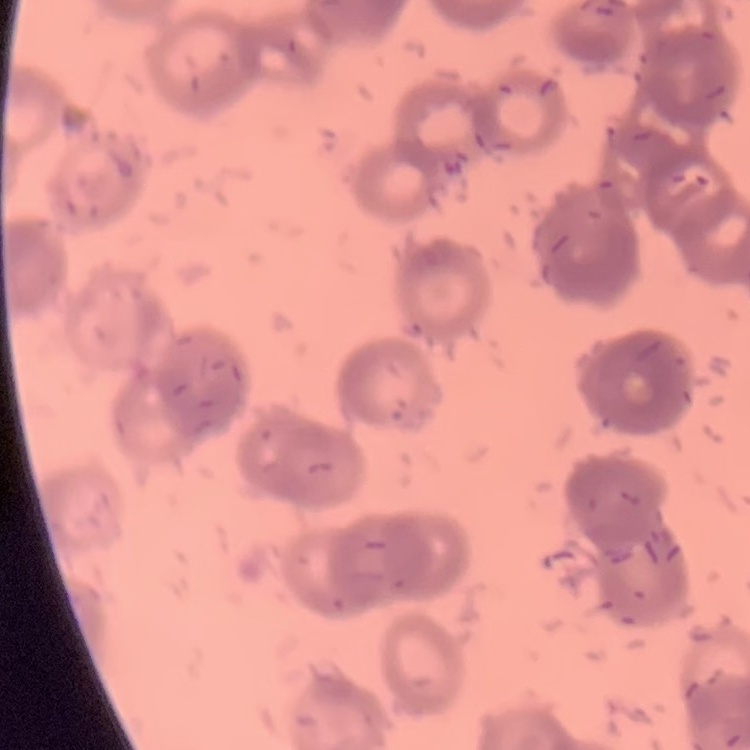
The erythrocytes exhibit rouleaux formation. Stained with either Field's or Giemsa. Thin blood film. Square crop of a larger photomicrograph.